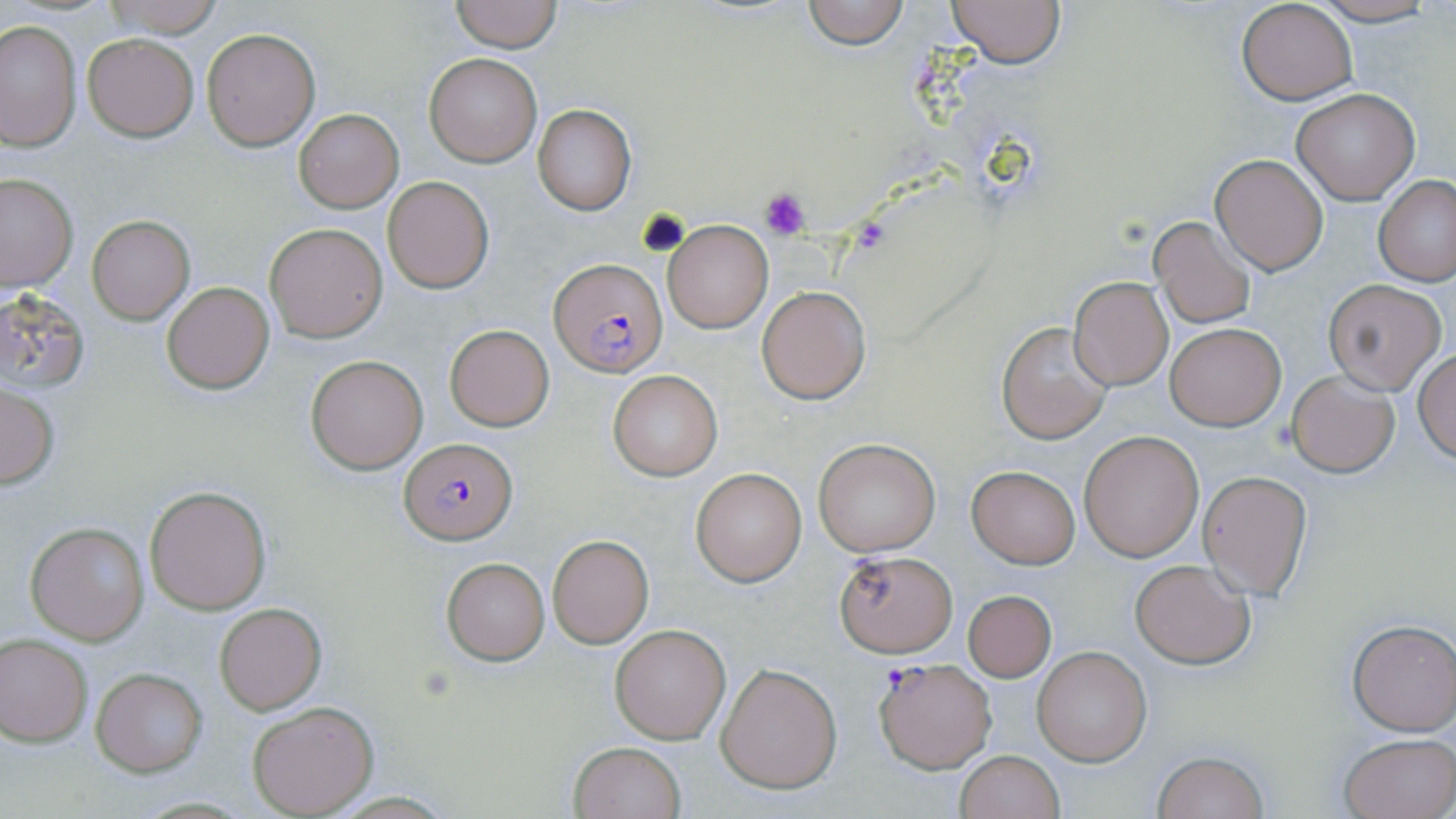
Summary:
  - Coordinate format: approximate bounding boxes as (x1, y1, x2, y2) in pixels
  - Uninfected red blood cell locations: (104, 0, 225, 39), (448, 0, 563, 51), (799, 0, 910, 49), (948, 0, 1066, 68), (1308, 0, 1440, 26), (1235, 1, 1357, 107), (0, 19, 80, 152), (201, 27, 322, 150), (82, 34, 198, 141), (425, 53, 540, 167), (1290, 88, 1418, 205), (533, 104, 637, 214), (293, 109, 403, 212), (1211, 155, 1328, 275), (0, 171, 77, 291), (383, 175, 495, 293), (1374, 175, 1455, 287), (1148, 215, 1257, 330), (87, 216, 194, 324), (663, 220, 771, 333), (266, 223, 388, 342), (1069, 277, 1172, 390), (1324, 279, 1446, 394), (161, 283, 275, 393), (755, 284, 871, 404), (0, 289, 92, 395), (997, 320, 1115, 444), (1165, 323, 1285, 430), (444, 325, 554, 430), (1413, 348, 1456, 464), (305, 354, 428, 474), (607, 370, 723, 480), (1285, 371, 1400, 478), (0, 385, 60, 488), (1078, 429, 1203, 561), (813, 438, 941, 557), (967, 465, 1080, 566), (691, 467, 806, 585), (1197, 470, 1313, 599), (144, 485, 273, 615), (26, 523, 148, 644), (548, 534, 653, 647), (834, 550, 956, 656), (441, 557, 549, 664), (1128, 559, 1256, 670), (962, 589, 1056, 682), (214, 603, 325, 714), (1348, 620, 1456, 736), (610, 624, 730, 744), (0, 636, 93, 745), (1032, 645, 1151, 766), (715, 662, 841, 794), (91, 668, 206, 776), (247, 700, 378, 816), (1338, 732, 1456, 818), (569, 741, 686, 819), (955, 750, 1064, 819), (1152, 750, 1270, 819)
  - Plasmodium falciparum-infected red blood cell locations: (549, 258, 666, 376), (399, 438, 517, 545), (873, 656, 996, 773)
  - Platelet locations: (760, 187, 813, 238), (639, 208, 689, 258)
  - Slide-level diagnosis: Plasmodium falciparum
  - Preparation: thin blood smear
  - Magnification: 1000x
  - Stain: May-Grünwald-Giemsa
  - Image size: 1456×819 pixels
  - Field of view: single
  - Modality: light microscopy